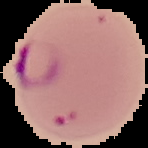
image type = segmented cell region with the area outside set to black
malaria status = parasitized
image size = 148×148 pixels
preparation = thin blood film